Report the malaria status of this cell.
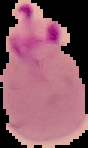

Parasitized.

Summary:
  - Image type: segmented cell region with the area outside set to black
  - Image size: 88×148 pixels
  - Preparation: thin blood film